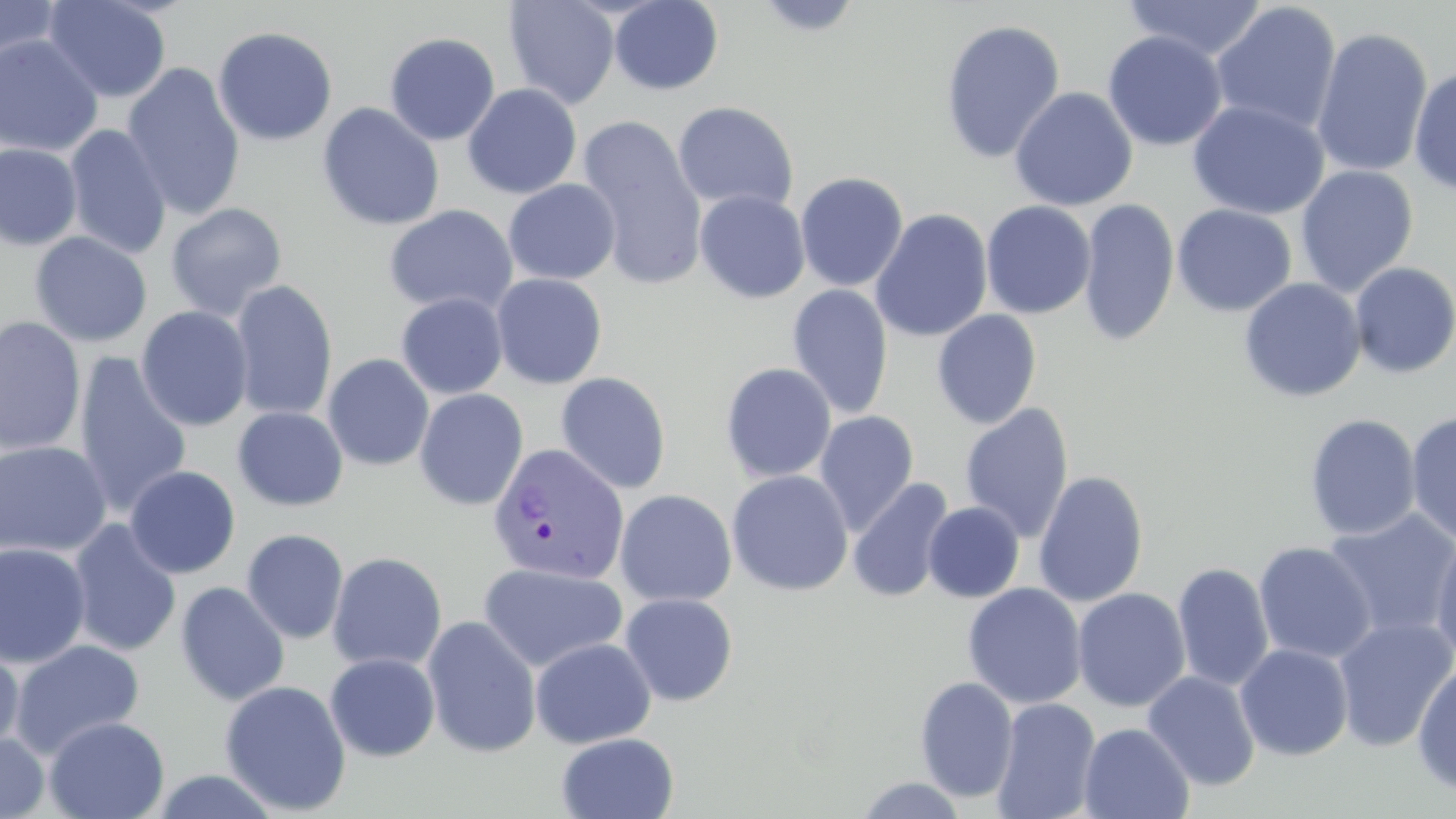 Approximate bounding boxes as named x1/y1/x2/y2 corners in pixels. Uninfected red blood cell locations: (x1=43, y1=0, x2=172, y2=103), (x1=502, y1=0, x2=620, y2=109), (x1=1123, y1=0, x2=1268, y2=62), (x1=0, y1=1, x2=64, y2=66), (x1=609, y1=1, x2=723, y2=95), (x1=751, y1=1, x2=866, y2=37), (x1=1209, y1=2, x2=1342, y2=136), (x1=939, y1=18, x2=1066, y2=164), (x1=212, y1=25, x2=338, y2=146), (x1=1311, y1=26, x2=1433, y2=179), (x1=384, y1=31, x2=501, y2=145), (x1=1102, y1=31, x2=1228, y2=152), (x1=0, y1=34, x2=104, y2=157), (x1=121, y1=62, x2=246, y2=221), (x1=1409, y1=65, x2=1456, y2=196), (x1=462, y1=83, x2=583, y2=199), (x1=1009, y1=86, x2=1138, y2=211), (x1=1187, y1=100, x2=1330, y2=219), (x1=672, y1=101, x2=799, y2=213), (x1=317, y1=102, x2=444, y2=231), (x1=575, y1=115, x2=708, y2=289), (x1=64, y1=124, x2=171, y2=259), (x1=0, y1=143, x2=82, y2=251), (x1=1295, y1=165, x2=1419, y2=296), (x1=794, y1=171, x2=909, y2=292), (x1=503, y1=179, x2=621, y2=285), (x1=694, y1=190, x2=810, y2=303), (x1=1078, y1=197, x2=1179, y2=348), (x1=980, y1=200, x2=1096, y2=319), (x1=165, y1=202, x2=288, y2=321), (x1=384, y1=204, x2=518, y2=316), (x1=1172, y1=204, x2=1297, y2=316), (x1=870, y1=208, x2=993, y2=343), (x1=29, y1=231, x2=152, y2=347), (x1=1349, y1=261, x2=1456, y2=379), (x1=491, y1=273, x2=608, y2=389), (x1=1239, y1=278, x2=1366, y2=403), (x1=230, y1=281, x2=338, y2=421), (x1=787, y1=284, x2=894, y2=420), (x1=396, y1=293, x2=508, y2=399), (x1=136, y1=305, x2=254, y2=432), (x1=931, y1=309, x2=1042, y2=429), (x1=0, y1=316, x2=86, y2=457), (x1=73, y1=352, x2=193, y2=518), (x1=322, y1=353, x2=435, y2=471), (x1=720, y1=362, x2=837, y2=483), (x1=555, y1=371, x2=672, y2=494), (x1=413, y1=388, x2=529, y2=511), (x1=959, y1=402, x2=1075, y2=544), (x1=232, y1=406, x2=348, y2=511), (x1=814, y1=409, x2=920, y2=535), (x1=1405, y1=411, x2=1456, y2=544), (x1=1304, y1=413, x2=1421, y2=541), (x1=0, y1=441, x2=113, y2=558), (x1=124, y1=465, x2=241, y2=579), (x1=726, y1=469, x2=853, y2=596), (x1=1033, y1=470, x2=1149, y2=608), (x1=847, y1=477, x2=954, y2=602), (x1=614, y1=489, x2=737, y2=608), (x1=923, y1=501, x2=1024, y2=603), (x1=1322, y1=508, x2=1456, y2=643), (x1=67, y1=519, x2=182, y2=657), (x1=241, y1=529, x2=349, y2=644), (x1=1429, y1=531, x2=1456, y2=665), (x1=0, y1=541, x2=92, y2=668), (x1=1253, y1=541, x2=1377, y2=664), (x1=327, y1=552, x2=447, y2=672), (x1=478, y1=562, x2=628, y2=673), (x1=1172, y1=562, x2=1274, y2=692), (x1=174, y1=581, x2=290, y2=706), (x1=962, y1=582, x2=1087, y2=709), (x1=1072, y1=588, x2=1191, y2=712), (x1=619, y1=592, x2=739, y2=706), (x1=422, y1=615, x2=542, y2=758), (x1=1332, y1=616, x2=1456, y2=752), (x1=530, y1=637, x2=656, y2=748), (x1=9, y1=639, x2=145, y2=760), (x1=0, y1=642, x2=25, y2=757), (x1=1235, y1=643, x2=1354, y2=761), (x1=324, y1=653, x2=440, y2=762), (x1=1412, y1=660, x2=1456, y2=797), (x1=1142, y1=670, x2=1261, y2=791), (x1=914, y1=676, x2=1019, y2=802), (x1=220, y1=680, x2=352, y2=815), (x1=991, y1=698, x2=1101, y2=819), (x1=44, y1=715, x2=169, y2=819), (x1=1079, y1=722, x2=1194, y2=819), (x1=556, y1=732, x2=679, y2=819), (x1=0, y1=733, x2=50, y2=819), (x1=148, y1=769, x2=283, y2=819), (x1=853, y1=777, x2=969, y2=818). Plasmodium vivax-infected red blood cell locations: (x1=486, y1=442, x2=629, y2=585). Slide-level diagnosis: Plasmodium vivax. Single field of view. Captured at 1000x magnification. May-Grünwald-Giemsa stain. Light microscopy. Thin blood film. Image is 1456×819 pixels.